Locate every leukocyte (white blood cell).
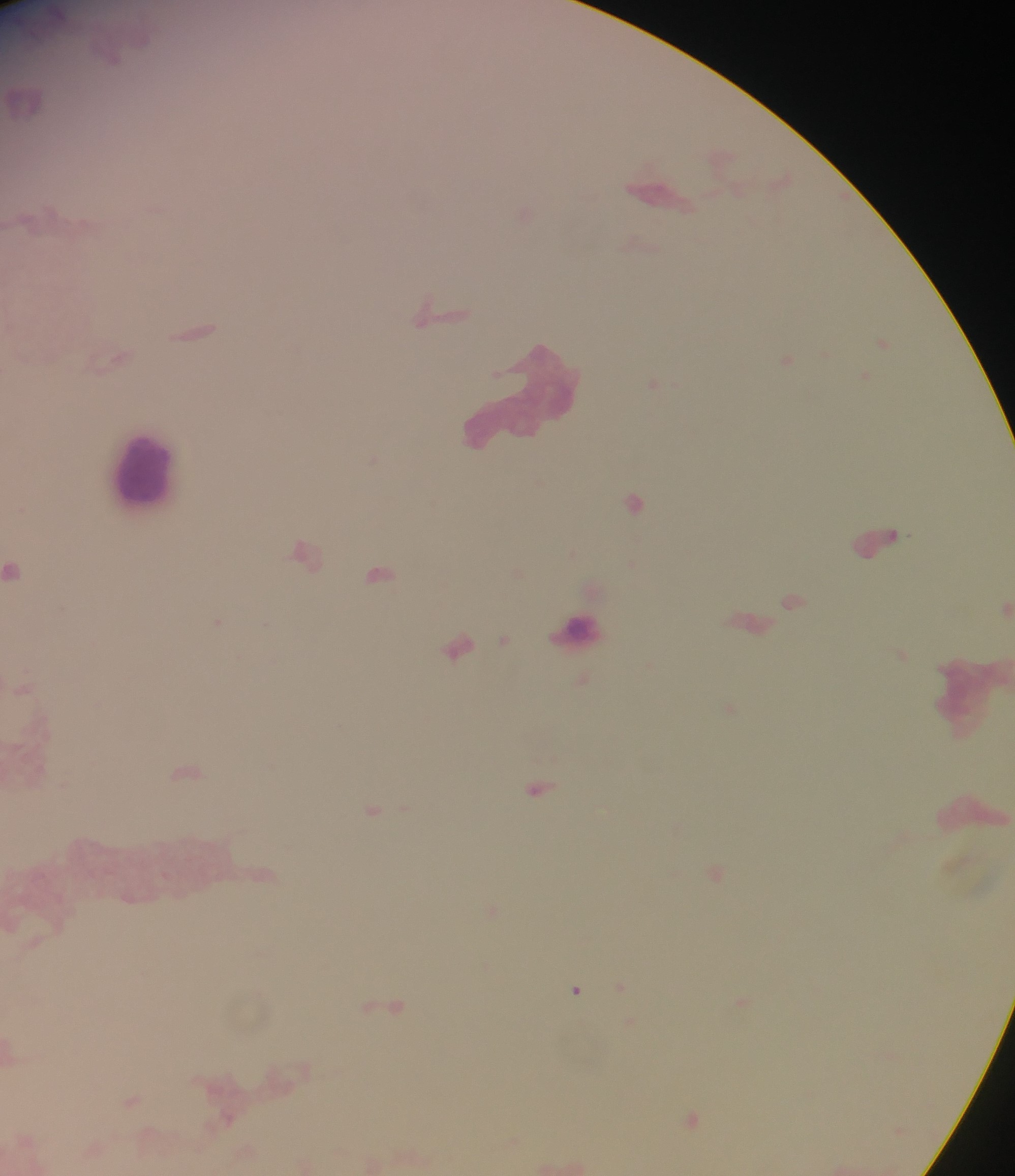

Approximate centers as (x, y) in pixels.
Leukocytes: (660, 194), (523, 399), (145, 469), (878, 542), (577, 630), (459, 647), (968, 699), (975, 812).

Malaria parasite locations: (196, 331), (883, 343), (787, 360), (652, 385), (373, 459), (633, 501), (304, 554), (15, 570), (380, 573), (791, 601), (1005, 608), (219, 621), (503, 640), (186, 772), (538, 789), (373, 811), (716, 872), (621, 987), (576, 990), (386, 1005), (133, 1101), (691, 1120). Single field of view. Mobile-phone photograph taken through the microscope. Image is 1015×1176 pixels. Collected in Ghana. Thick blood smear.